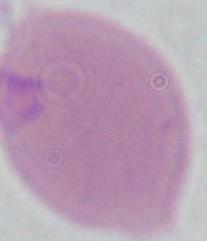

Summary:
  - Magnification: 1000x
  - Modality: micrograph
  - Identification: red blood cell